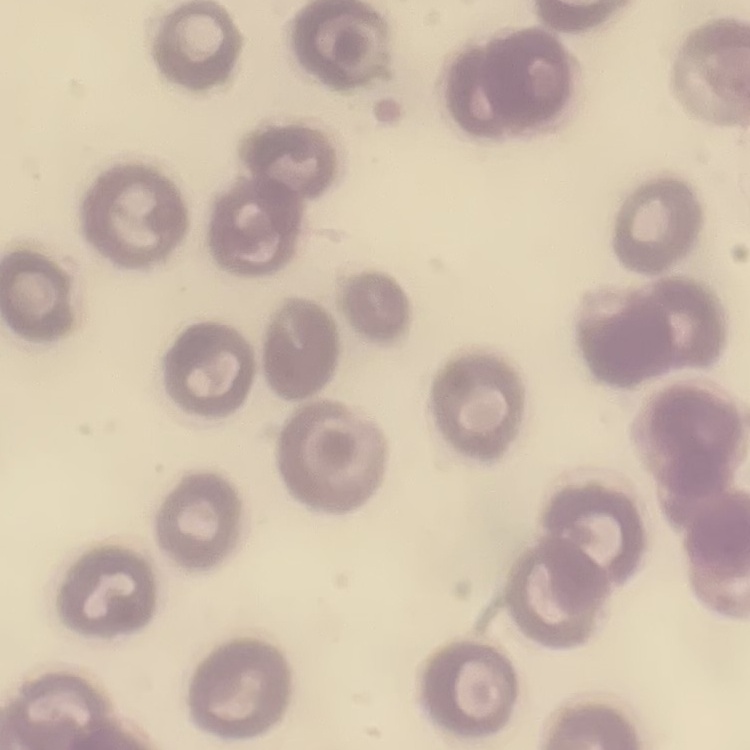

The erythrocytes exhibit no rouleaux formation. One tile cut from a larger photomicrograph. Stained with either Field's or Giemsa. Thin blood film.